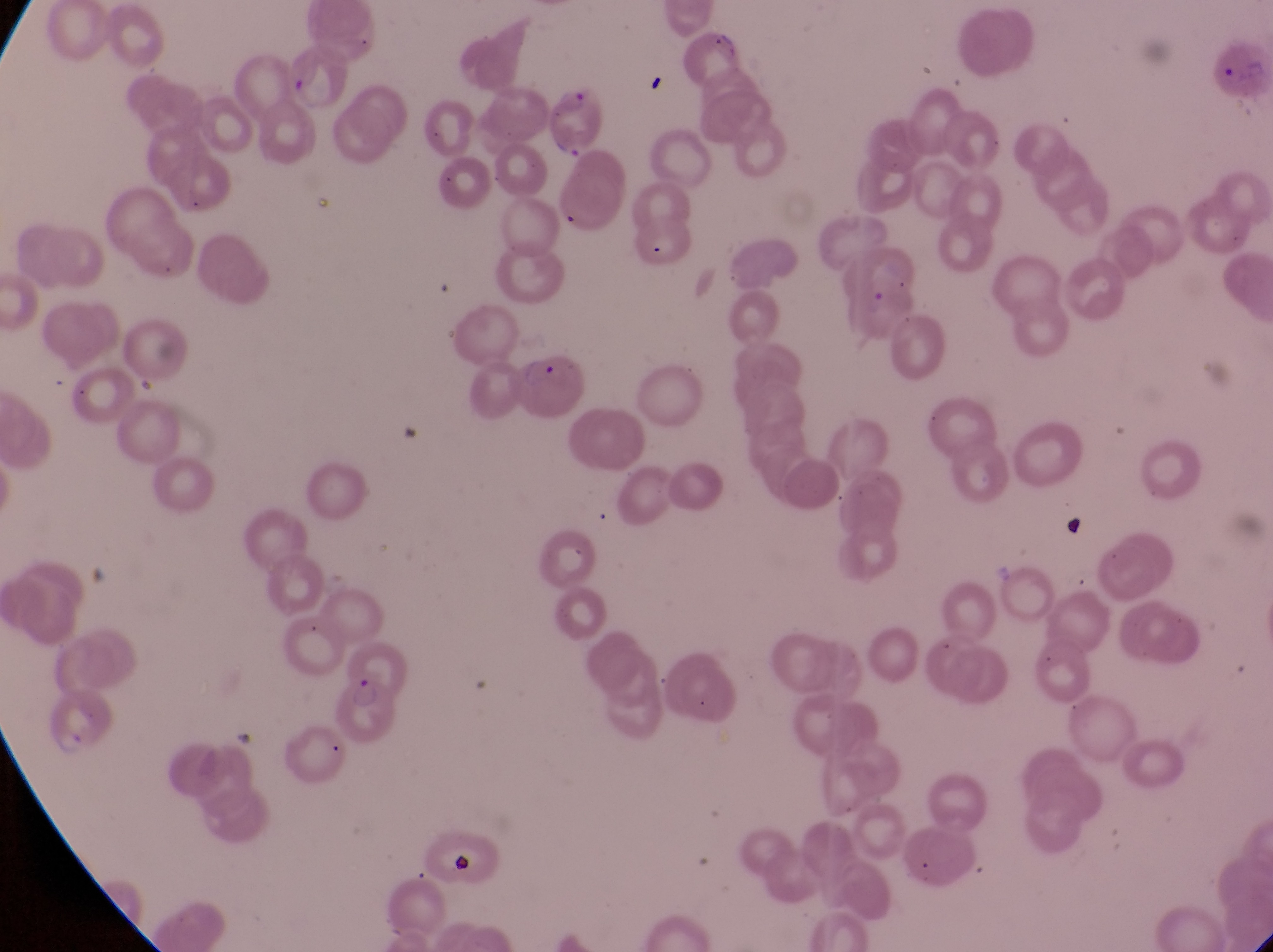
Approximate bounding boxes as {left, top, right, bottom} in pixels. Artifact (platelet-like body, stain precipitate, or debris) locations: {1056, 509, 1095, 548}, {444, 842, 487, 892}. Parasitised red blood cell locations: {544, 77, 613, 157}, {334, 675, 396, 740}. Image is 1273×952 pixels. Photographed through the eyepiece of an Olympus CX-23 microscope with a smartphone camera. Collected in Uganda. One field of view. Thin blood film. Magnification of 1000x.